Classify this cell by malaria status.
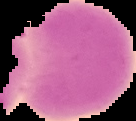
It is uninfected.

Summary:
  - Image size: 136×121 pixels
  - Image type: segmented cell region with the area outside set to black
  - Preparation: thin blood smear